Identify the preparation type.
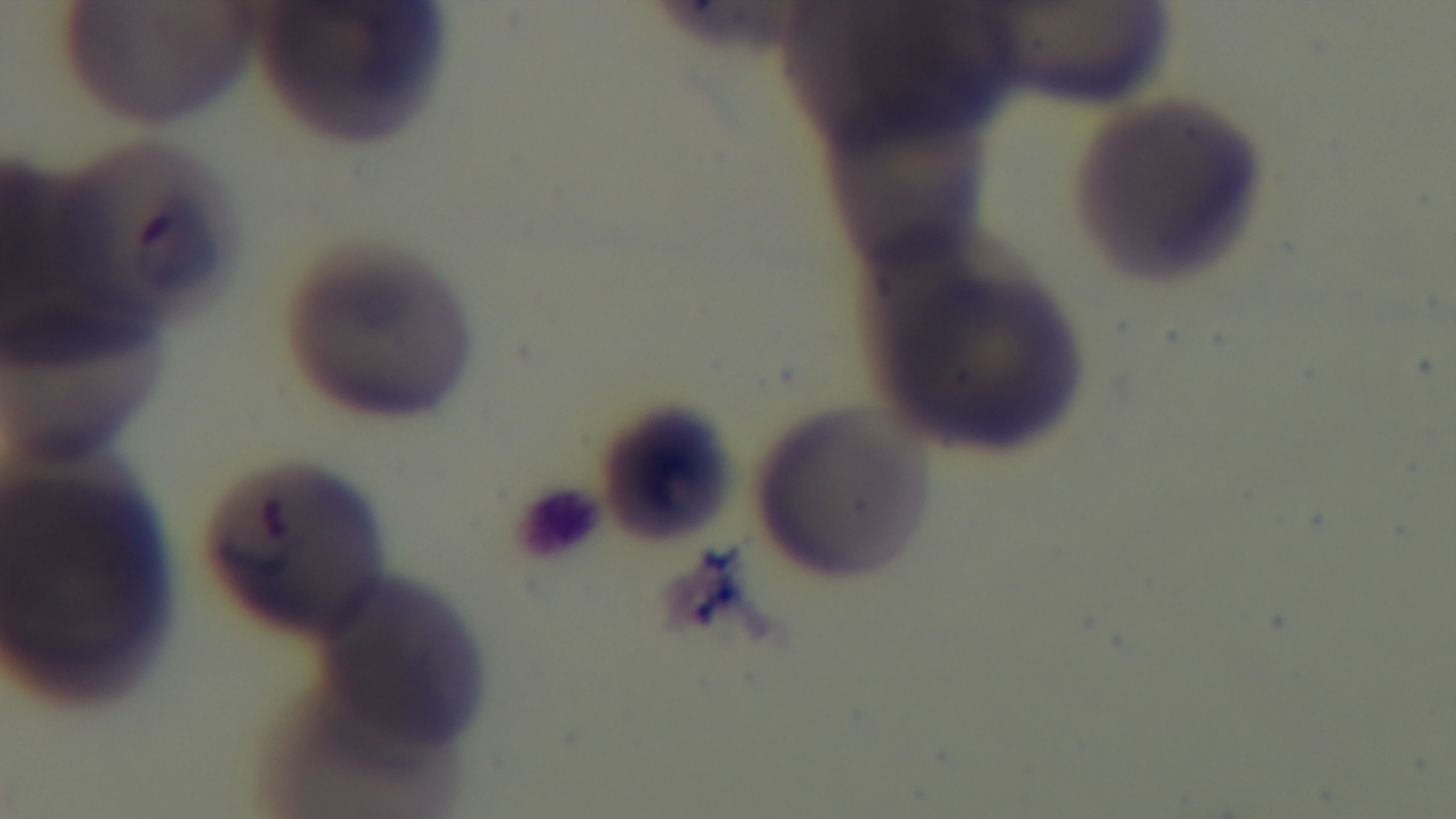

A thin smear.

Malaria status: positive. Light microscopy. One field from the slide. 100x oil-immersion objective. Giemsa-stained. Captured with a mounted 4K digital camera.